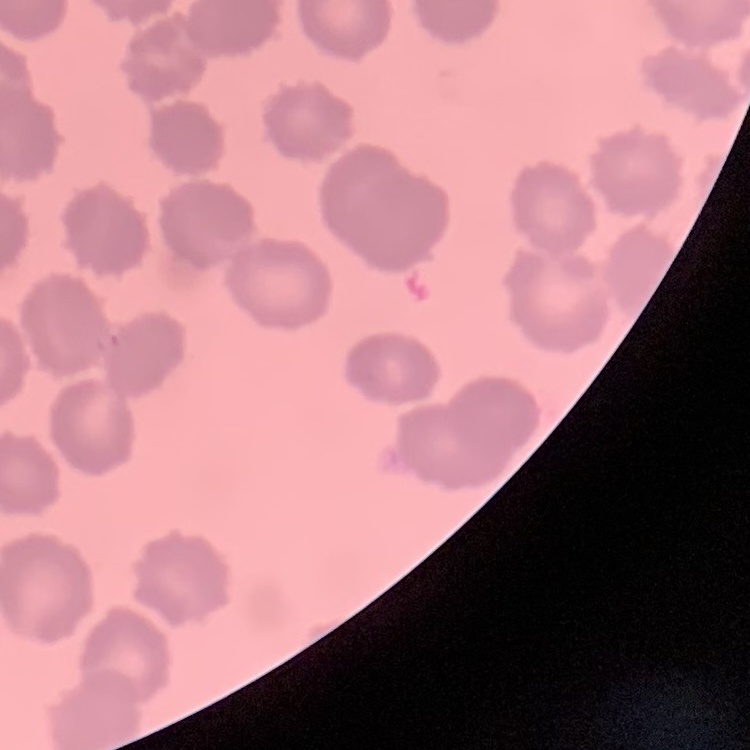

The erythrocytes exhibit no rouleaux formation. Stained with either Field's or Giemsa. Square crop of a larger photomicrograph. Thin peripheral smear.